Identify the parasite.
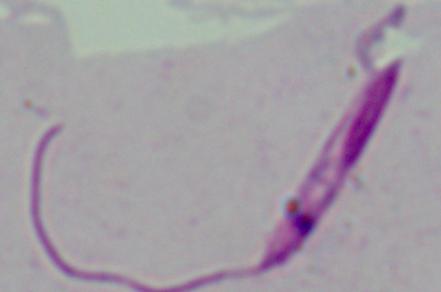
This is Leishmania.

Summary:
  - Modality: photomicrograph
  - Magnification: 1000x